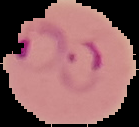

preparation = thin blood smear
image type = segmented cell region with the area outside set to black
image size = 139×127 pixels
result = malaria parasites identified